Identify the blood parasite species.
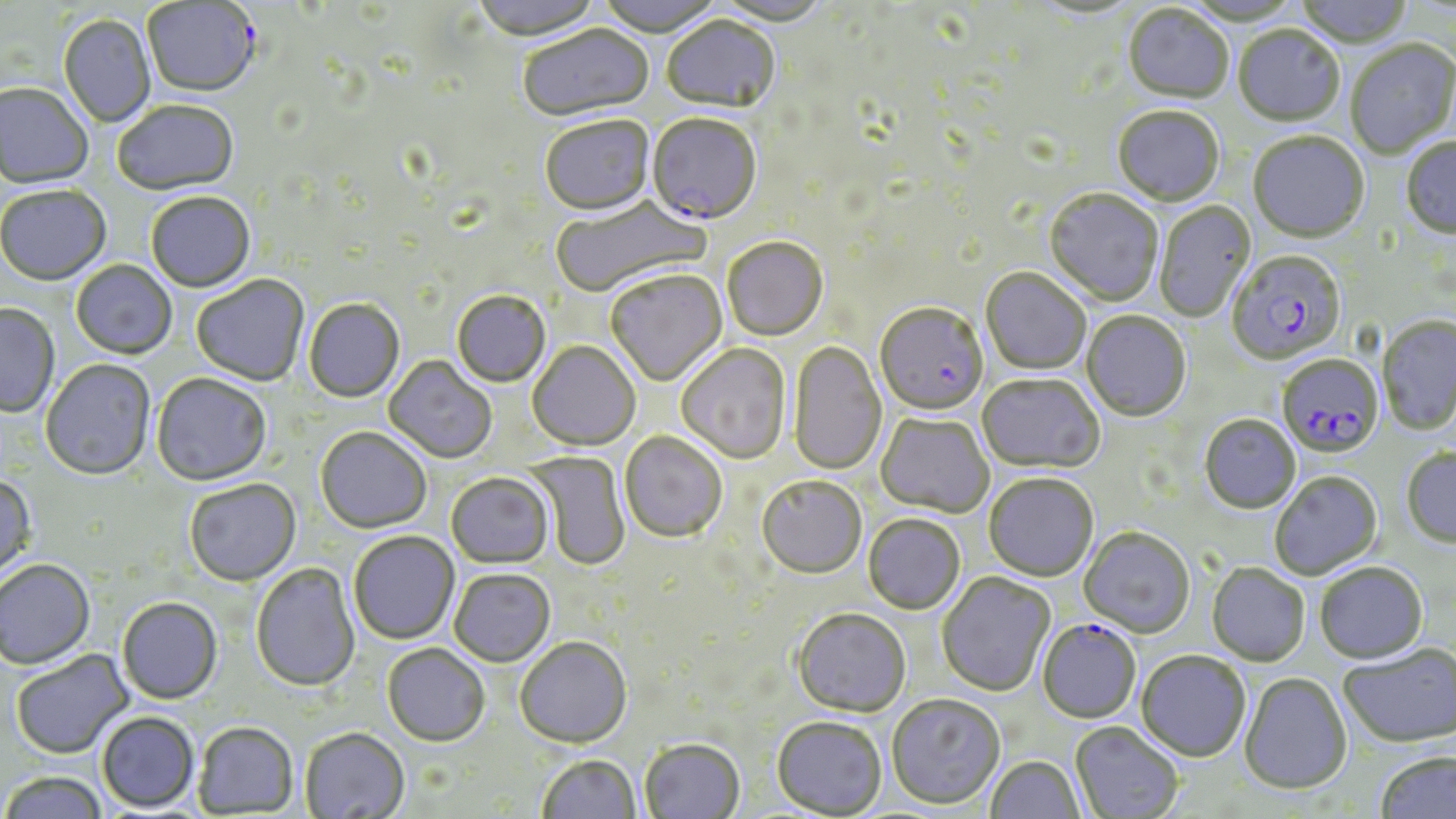
Plasmodium falciparum.

Approximate bounding boxes as (x1,y1)-(x2,y2) corner pairs in pixels. Plasmodium falciparum-infected red blood cell locations: (142,1)-(261,99), (646,116)-(761,227), (1226,252)-(1347,366), (875,305)-(988,418), (1277,356)-(1383,460), (1037,621)-(1141,725). Uninfected red blood cell locations: (471,0)-(602,44), (594,0)-(726,39), (712,0)-(831,28), (1293,0)-(1413,51), (1029,1)-(1142,22), (1183,1)-(1304,27), (1122,6)-(1234,106), (58,15)-(155,128), (661,17)-(781,117), (519,26)-(655,125), (1233,27)-(1345,128), (1345,41)-(1456,160), (0,84)-(94,191), (112,102)-(240,197), (1112,108)-(1224,208), (540,118)-(655,219), (1248,133)-(1369,245), (1401,138)-(1456,240), (0,186)-(111,287), (1044,190)-(1163,307), (146,193)-(255,294), (549,196)-(708,300), (1154,202)-(1257,323), (722,239)-(828,342), (71,261)-(177,361), (980,269)-(1091,375), (606,271)-(727,388), (191,276)-(310,387), (451,292)-(551,389), (303,299)-(405,403), (0,304)-(60,418), (1081,312)-(1191,422), (1377,316)-(1456,436), (788,341)-(886,475), (527,342)-(641,452), (675,345)-(791,465), (383,356)-(497,464), (41,359)-(155,481), (151,374)-(273,487), (977,374)-(1104,475), (876,414)-(994,518), (1200,415)-(1301,515), (315,427)-(431,534), (619,432)-(728,544), (1401,449)-(1456,549), (524,450)-(630,570), (1270,472)-(1383,580), (445,473)-(554,570), (0,474)-(37,580), (984,474)-(1099,583), (756,478)-(867,581), (185,479)-(301,586), (863,515)-(965,616), (1079,528)-(1195,639), (349,532)-(460,645), (0,560)-(95,670), (250,563)-(360,692), (1315,563)-(1428,665), (1207,564)-(1310,667), (449,569)-(555,668), (937,572)-(1056,698), (117,597)-(222,704), (792,610)-(911,719), (515,639)-(632,749), (381,644)-(490,746), (1338,644)-(1456,749), (11,650)-(133,759), (1135,652)-(1250,763), (1239,674)-(1352,796), (886,695)-(1005,810), (97,711)-(200,813), (771,717)-(887,818), (193,721)-(299,816), (1069,722)-(1183,818), (299,727)-(410,819), (640,739)-(745,819), (1374,751)-(1456,819), (536,756)-(642,818), (985,756)-(1085,818), (0,772)-(109,819). Image is 1456×819 pixels. May-Grünwald-Giemsa stain. 1000x magnification. Optical microscopy. Thin blood film. One field of a larger specimen.